Name the parasite shown.
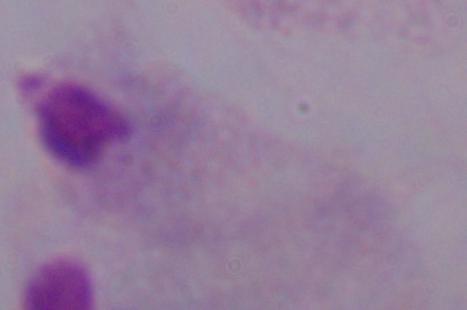
A trichomonad.

modality: photomicrograph
magnification: 1000x